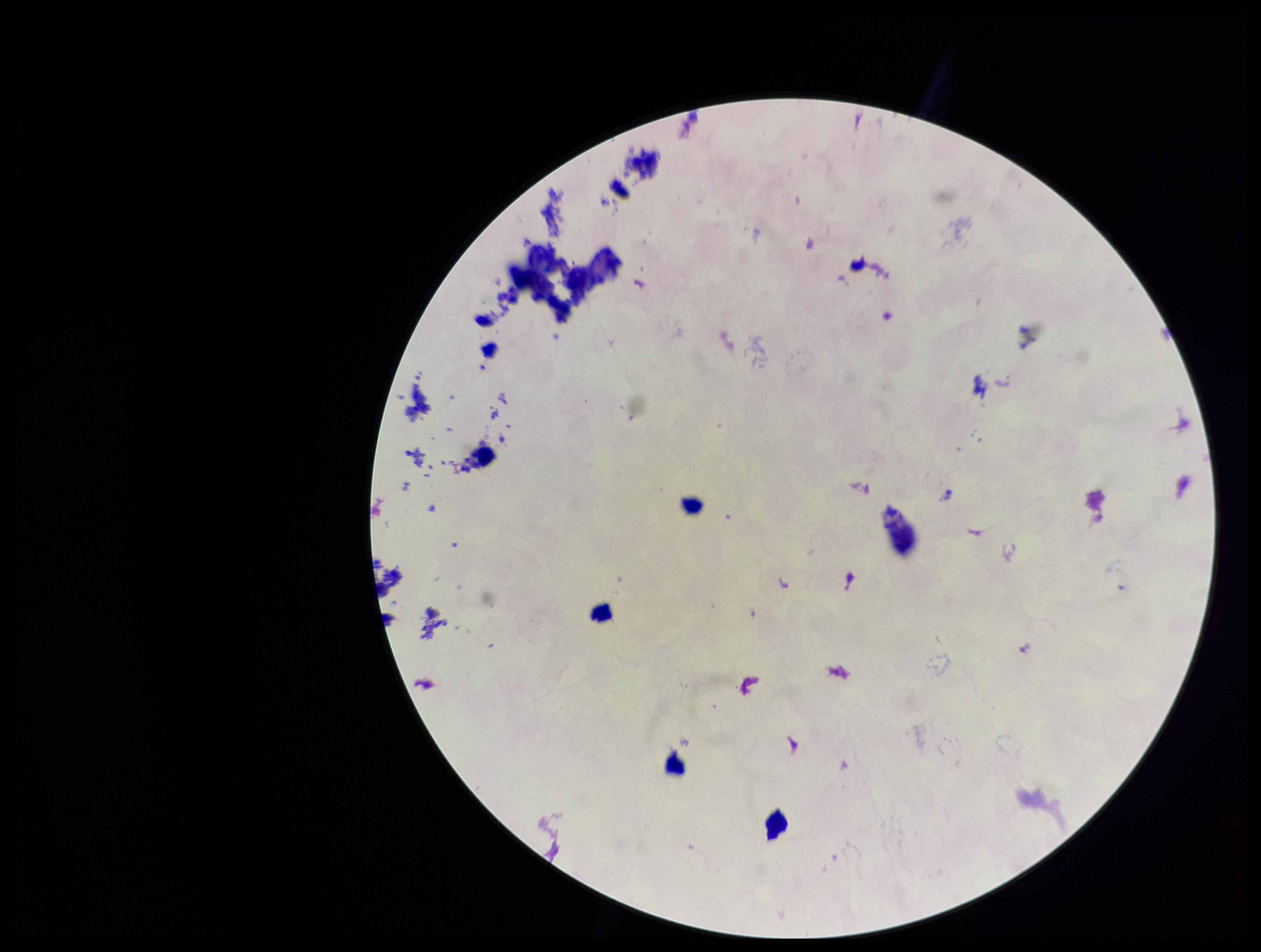
Summary:
  - Parasite count: 0
  - Plasmodium parasites: none identified
  - Preparation: thick blood smear
  - Field of view: one from this slide
  - Image size: 1261×952 pixels
  - Leukocyte count: 6
  - Stain: Giemsa
  - Patient malaria status: negative
  - Capture: smartphone photograph through the microscope eyepiece